Name the parasite shown.
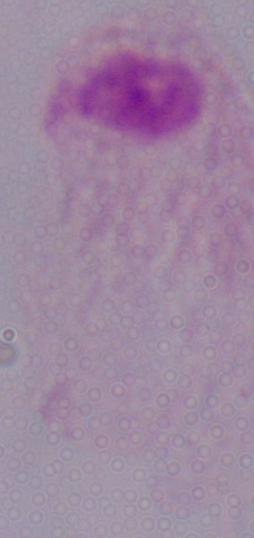
This is a trichomonad.

1000x magnification. Micrograph.